Locate every malaria parasite.
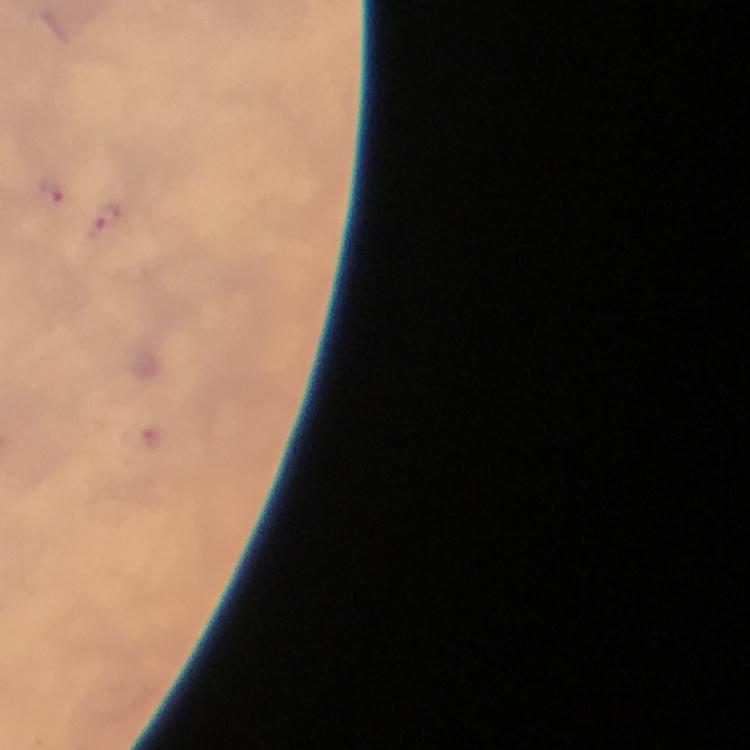
Approximate centers as (x, y) in pixels.
Malaria parasites: (52, 190), (103, 224).

Summary:
  - Capture: smartphone photograph through a microscope
  - Image size: 750×750 pixels
  - Stain: Giemsa
  - Magnification: 100x
  - Context: from a diagnostic examination for malaria
  - Immersion oil: applied
  - Cropped from: a single field of view
  - Preparation: thick smear